Assess the morphology of the erythrocytes.
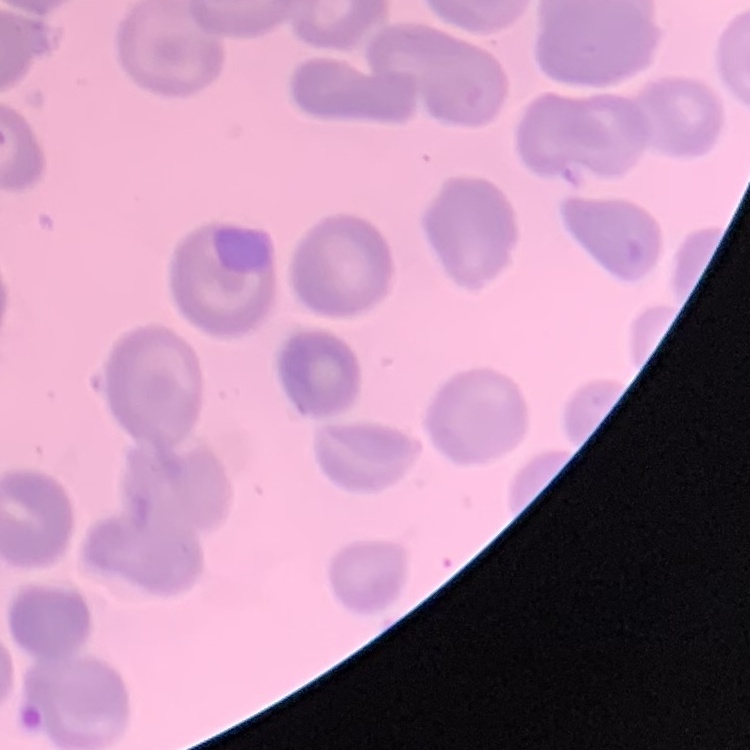
No rouleaux formation.

Thin peripheral smear. Field's or Giemsa stain. Square crop of a larger photomicrograph.